Assess this cell for malaria.
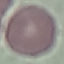
It is uninfected.

{
  "stain": "Giemsa",
  "capture": "smartphone camera at the microscope eyepiece",
  "image_type": "cell patch, automatically extracted from a larger field of view and resized to 64 × 64 pixels",
  "preparation": "thin blood film"
}